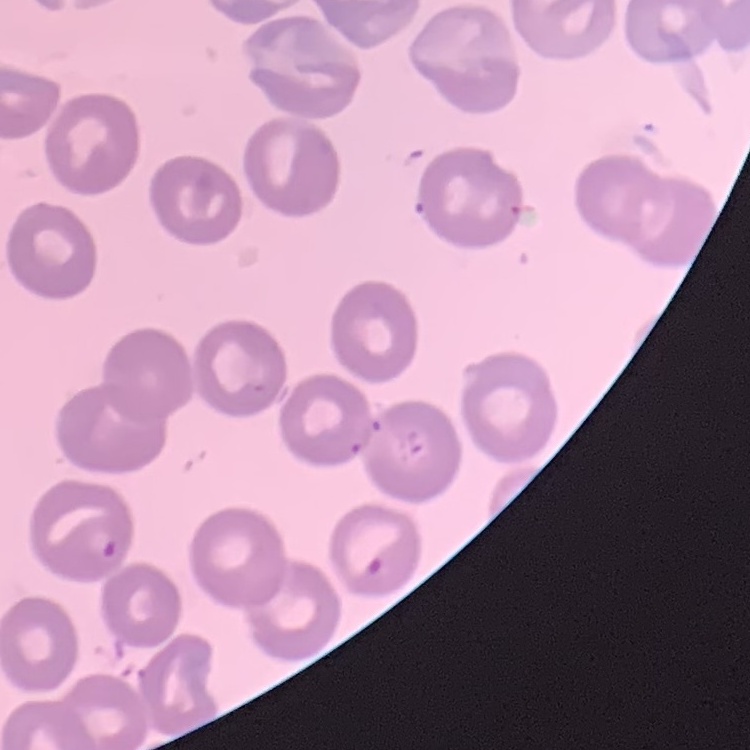

erythrocyte morphology = no rouleaux formation
stain = Field's or Giemsa
image type = square crop of a larger photomicrograph
preparation = thin peripheral smear